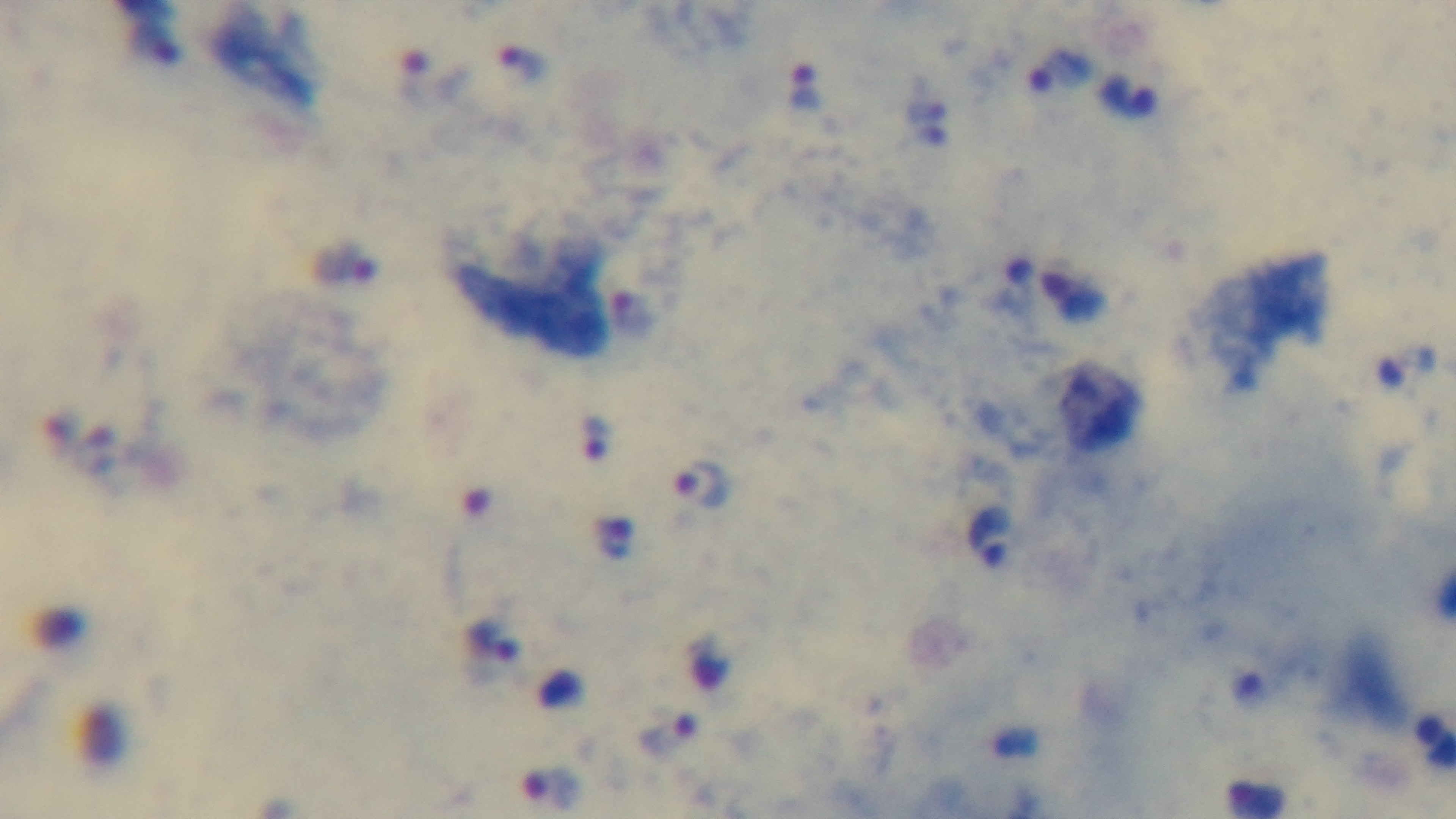
objective: 100x oil immersion
preparation: thick blood film
field_of_view: single
modality: light microscopy
stain: Giemsa
capture: mounted 4K digital camera
malaria_status: infected